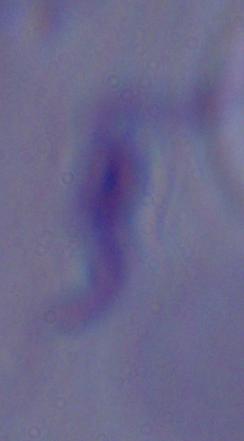

A trypanosome is seen. Micrograph. 1000x magnification.